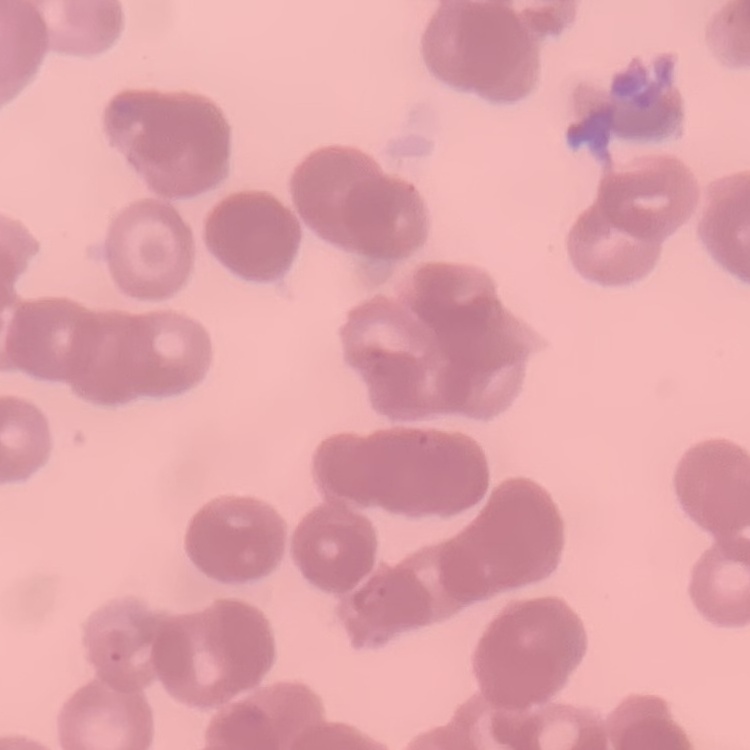
{
  "red_blood_cell_morphology": "rouleaux formation",
  "image_type": "one tile cut from a larger photomicrograph",
  "stain": "Field's or Giemsa",
  "preparation": "thin blood film"
}